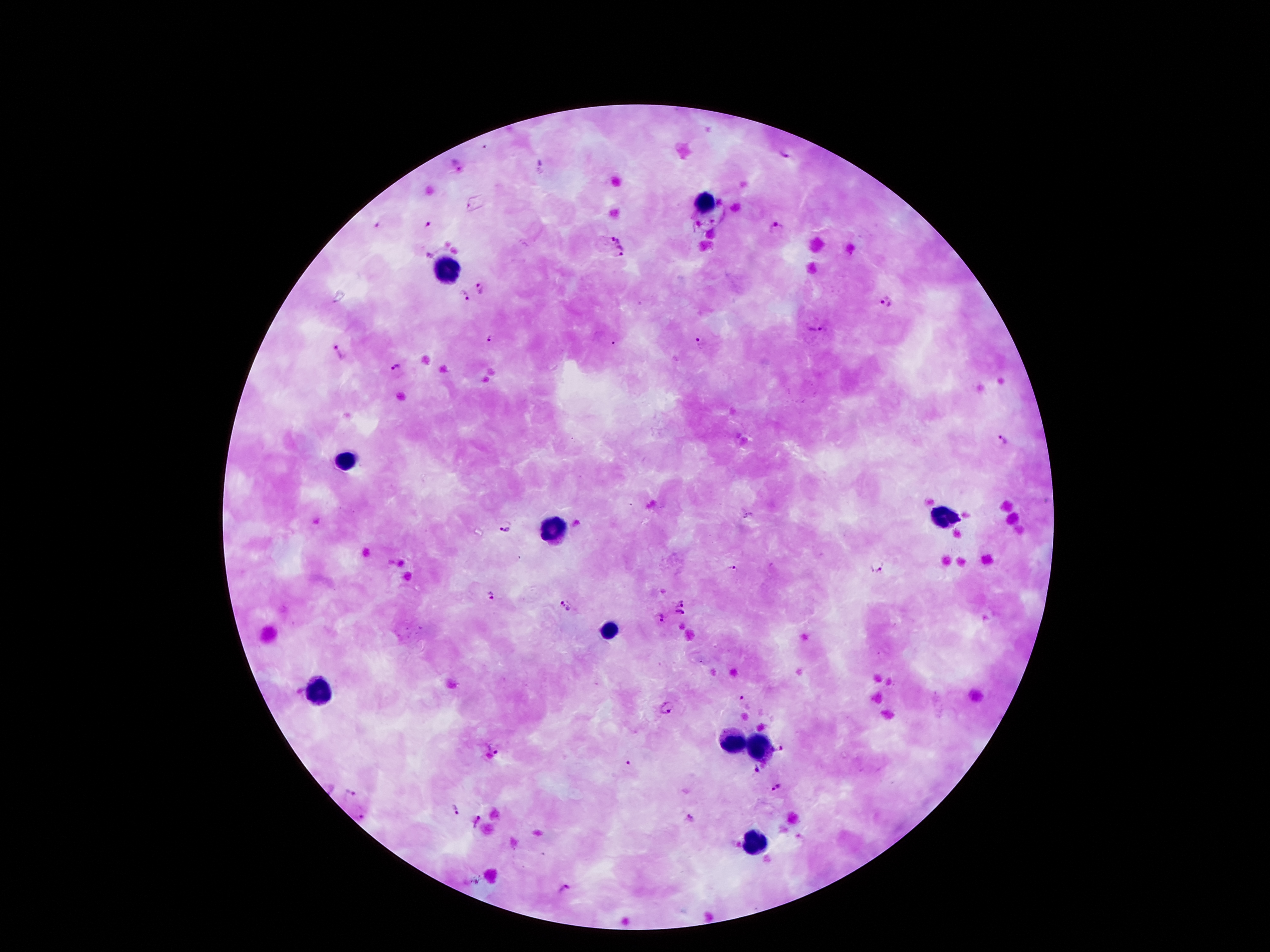
{
  "preparation": "thick blood smear",
  "plasmodium_parasite_locations": "approximate centers as {x, y} in pixels: {784, 154}, {542, 166}, {458, 167}, {379, 224}, {428, 225}, {777, 229}, {616, 235}, {621, 252}, {481, 288}, {463, 298}, {886, 302}, {817, 328}, {493, 339}, {701, 341}, {336, 352}, {397, 367}, {1003, 441}, {504, 526}, {878, 566}, {733, 567}, {491, 595}, {682, 600}, {566, 604}, {682, 612}, {661, 617}, {743, 699}, {667, 706}, {492, 746}, {783, 747}, {627, 766}, {756, 772}, {777, 788}, {348, 792}, {455, 811}, {364, 813}, {475, 823}, {562, 889}",
  "stain": "Giemsa",
  "leukocyte_locations": "approximate centers as {x, y} in pixels: {706, 205}, {447, 267}, {346, 461}, {942, 516}, {551, 531}, {613, 630}, {319, 692}, {734, 743}, {759, 748}, {756, 842}",
  "image_size": "1270×952 pixels",
  "capture": "smartphone camera through the microscope eyepiece",
  "magnification": "100x",
  "patient_malaria_status": "positive for Plasmodium falciparum",
  "field_of_view": "one from this slide"
}